Locate platelets.
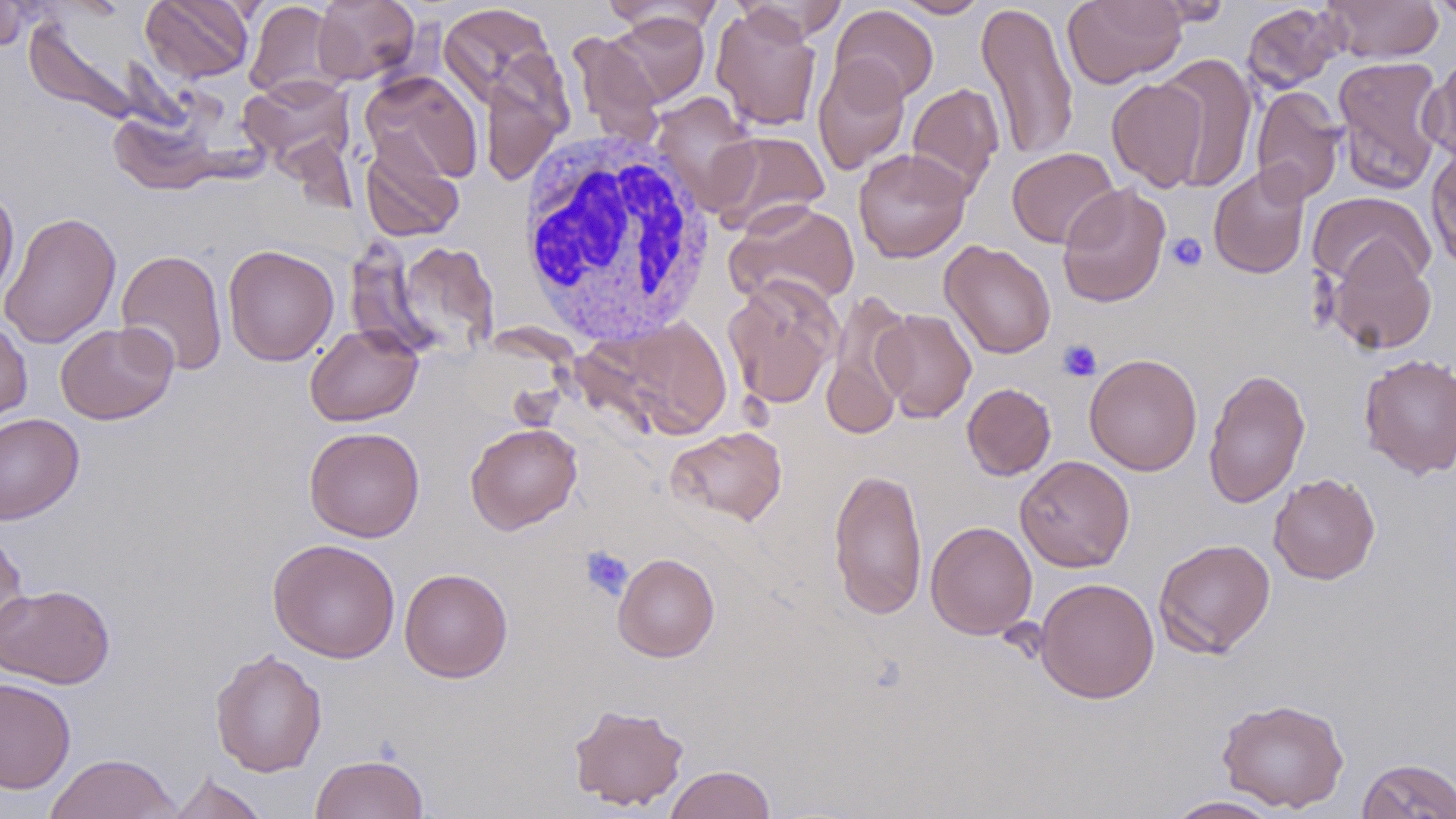

Approximate bounding boxes as named x1/y1/x2/y2 corners in pixels.
Platelets: (x1=1166, y1=232, x2=1208, y2=271), (x1=1057, y1=339, x2=1102, y2=382), (x1=579, y1=545, x2=634, y2=601).

slide-level diagnosis = no evidence of blood parasites
uninfected red blood cell locations = approximate bounding boxes as named x1/y1/x2/y2 corners in pixels: (x1=141, y1=0, x2=255, y2=83), (x1=312, y1=0, x2=420, y2=85), (x1=892, y1=0, x2=991, y2=18), (x1=1062, y1=0, x2=1187, y2=88), (x1=1147, y1=0, x2=1234, y2=26), (x1=1324, y1=0, x2=1443, y2=63), (x1=1428, y1=0, x2=1456, y2=24), (x1=0, y1=1, x2=36, y2=50), (x1=244, y1=1, x2=346, y2=101), (x1=733, y1=1, x2=849, y2=43), (x1=976, y1=1, x2=1080, y2=164), (x1=601, y1=2, x2=725, y2=39), (x1=1241, y1=2, x2=1345, y2=93), (x1=438, y1=3, x2=558, y2=108), (x1=830, y1=5, x2=939, y2=104), (x1=711, y1=6, x2=823, y2=132), (x1=606, y1=13, x2=710, y2=106), (x1=24, y1=15, x2=141, y2=125), (x1=567, y1=31, x2=666, y2=147), (x1=1157, y1=53, x2=1259, y2=192), (x1=479, y1=55, x2=573, y2=187), (x1=812, y1=55, x2=910, y2=175), (x1=1332, y1=56, x2=1449, y2=195), (x1=1421, y1=56, x2=1456, y2=169), (x1=360, y1=71, x2=482, y2=187), (x1=239, y1=74, x2=356, y2=170), (x1=1107, y1=77, x2=1210, y2=192), (x1=907, y1=82, x2=1004, y2=196), (x1=1251, y1=86, x2=1346, y2=205), (x1=651, y1=92, x2=760, y2=213), (x1=108, y1=108, x2=223, y2=195), (x1=709, y1=131, x2=830, y2=236), (x1=360, y1=139, x2=465, y2=243), (x1=1426, y1=144, x2=1456, y2=273), (x1=1006, y1=147, x2=1121, y2=249), (x1=853, y1=148, x2=972, y2=263), (x1=1208, y1=165, x2=1311, y2=279), (x1=1057, y1=183, x2=1171, y2=308), (x1=0, y1=186, x2=19, y2=302), (x1=1308, y1=192, x2=1435, y2=291), (x1=725, y1=199, x2=860, y2=310), (x1=0, y1=211, x2=121, y2=349), (x1=1324, y1=238, x2=1438, y2=354), (x1=387, y1=239, x2=500, y2=359), (x1=939, y1=240, x2=1057, y2=359), (x1=223, y1=244, x2=339, y2=366), (x1=116, y1=248, x2=228, y2=376), (x1=722, y1=276, x2=841, y2=409), (x1=821, y1=290, x2=917, y2=439), (x1=872, y1=309, x2=977, y2=422), (x1=0, y1=317, x2=32, y2=425), (x1=607, y1=317, x2=732, y2=439), (x1=55, y1=321, x2=178, y2=425), (x1=305, y1=323, x2=423, y2=426), (x1=1083, y1=353, x2=1202, y2=476), (x1=1359, y1=353, x2=1456, y2=479), (x1=1203, y1=367, x2=1311, y2=509), (x1=962, y1=383, x2=1056, y2=481), (x1=0, y1=413, x2=84, y2=524), (x1=465, y1=422, x2=582, y2=534), (x1=665, y1=425, x2=788, y2=527), (x1=304, y1=426, x2=424, y2=542), (x1=1015, y1=455, x2=1135, y2=573), (x1=828, y1=466, x2=928, y2=620), (x1=1268, y1=473, x2=1380, y2=584), (x1=925, y1=520, x2=1038, y2=639), (x1=0, y1=528, x2=31, y2=657), (x1=267, y1=538, x2=401, y2=663), (x1=1153, y1=538, x2=1276, y2=659), (x1=612, y1=552, x2=720, y2=662), (x1=399, y1=567, x2=513, y2=683), (x1=1035, y1=576, x2=1160, y2=704), (x1=0, y1=583, x2=115, y2=689), (x1=210, y1=648, x2=327, y2=777), (x1=0, y1=677, x2=76, y2=794), (x1=1217, y1=697, x2=1349, y2=813), (x1=568, y1=703, x2=689, y2=811), (x1=44, y1=753, x2=181, y2=818), (x1=310, y1=753, x2=429, y2=819), (x1=1357, y1=757, x2=1456, y2=818), (x1=664, y1=765, x2=776, y2=819), (x1=164, y1=772, x2=270, y2=819), (x1=1164, y1=795, x2=1284, y2=818)
stain = May-Grünwald-Giemsa
white blood cell locations = approximate bounding boxes as named x1/y1/x2/y2 corners in pixels: (x1=516, y1=128, x2=718, y2=344)
preparation = thin blood film
field of view = one of a larger specimen
magnification = 1000x
modality = light microscopy
image size = 1456×819 pixels